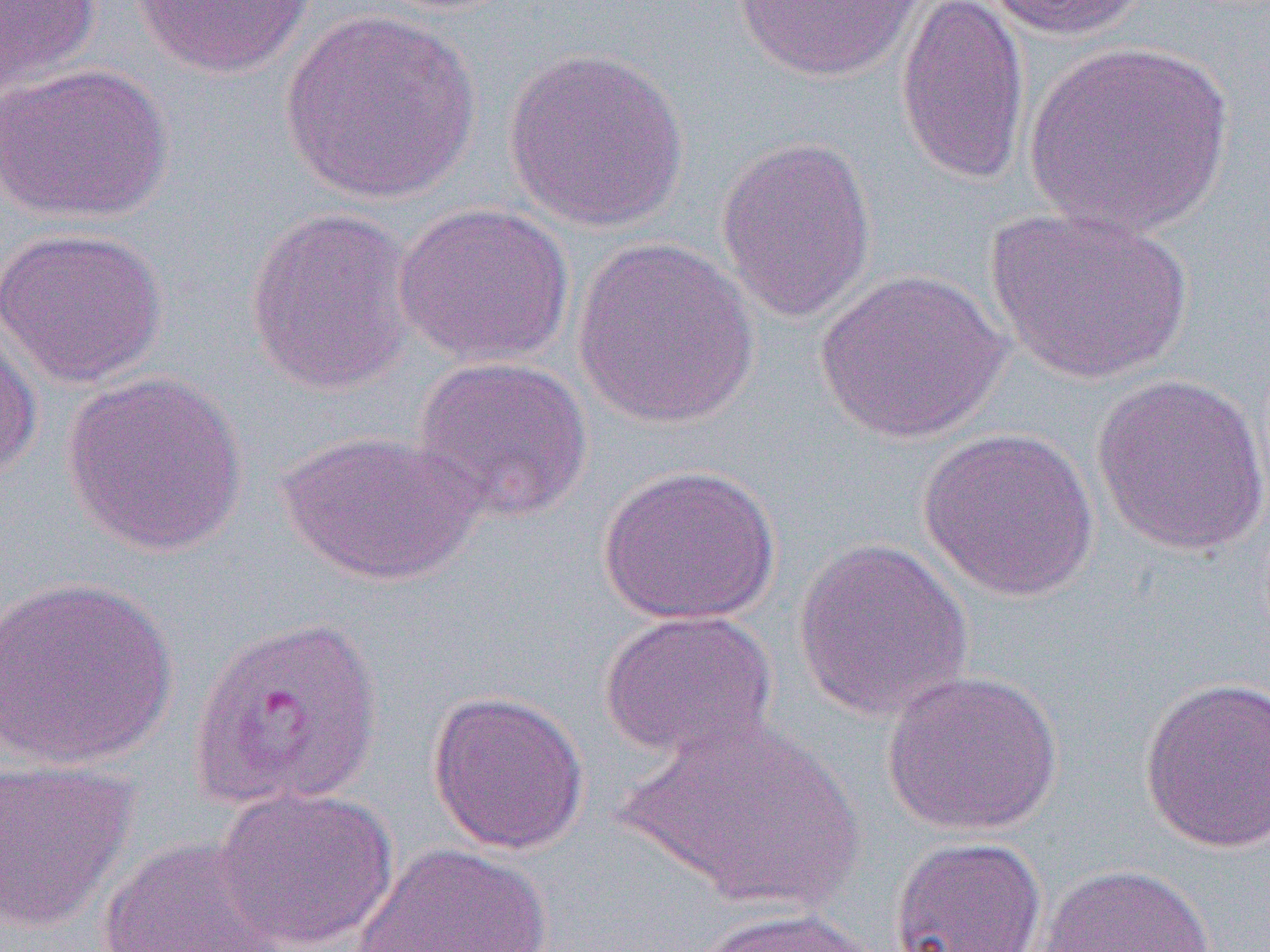
Summary:
  - Coordinate format: approximate bounding boxes as named x1/y1/x2/y2 corners in pixels
  - Uninfected red blood cell locations: (x1=0, y1=0, x2=101, y2=98), (x1=732, y1=0, x2=931, y2=82), (x1=894, y1=0, x2=1031, y2=187), (x1=979, y1=0, x2=1151, y2=41), (x1=131, y1=1, x2=317, y2=78), (x1=280, y1=7, x2=481, y2=204), (x1=1024, y1=40, x2=1233, y2=238), (x1=503, y1=47, x2=690, y2=232), (x1=0, y1=61, x2=171, y2=226), (x1=716, y1=135, x2=878, y2=324), (x1=393, y1=200, x2=575, y2=368), (x1=244, y1=205, x2=419, y2=396), (x1=984, y1=206, x2=1194, y2=386), (x1=0, y1=226, x2=167, y2=388), (x1=571, y1=235, x2=760, y2=429), (x1=814, y1=268, x2=1011, y2=444), (x1=0, y1=317, x2=42, y2=481), (x1=411, y1=354, x2=594, y2=524), (x1=60, y1=370, x2=248, y2=558), (x1=1092, y1=372, x2=1270, y2=557), (x1=917, y1=427, x2=1100, y2=602), (x1=278, y1=429, x2=482, y2=586), (x1=597, y1=463, x2=782, y2=626), (x1=793, y1=537, x2=974, y2=722), (x1=0, y1=576, x2=179, y2=770), (x1=599, y1=609, x2=777, y2=762), (x1=882, y1=667, x2=1063, y2=837), (x1=1138, y1=675, x2=1269, y2=854), (x1=427, y1=689, x2=590, y2=855), (x1=620, y1=714, x2=865, y2=913), (x1=0, y1=758, x2=138, y2=933), (x1=213, y1=784, x2=399, y2=951), (x1=889, y1=835, x2=1047, y2=952), (x1=97, y1=836, x2=288, y2=951), (x1=348, y1=843, x2=560, y2=952), (x1=1033, y1=862, x2=1217, y2=952), (x1=687, y1=906, x2=887, y2=952)
  - Slide-level diagnosis: Plasmodium vivax
  - Magnification: 1000x
  - Image size: 1270×952 pixels
  - Field of view: single
  - Modality: optical microscopy
  - Preparation: thin blood film